Locate every uninfected red blood cell.
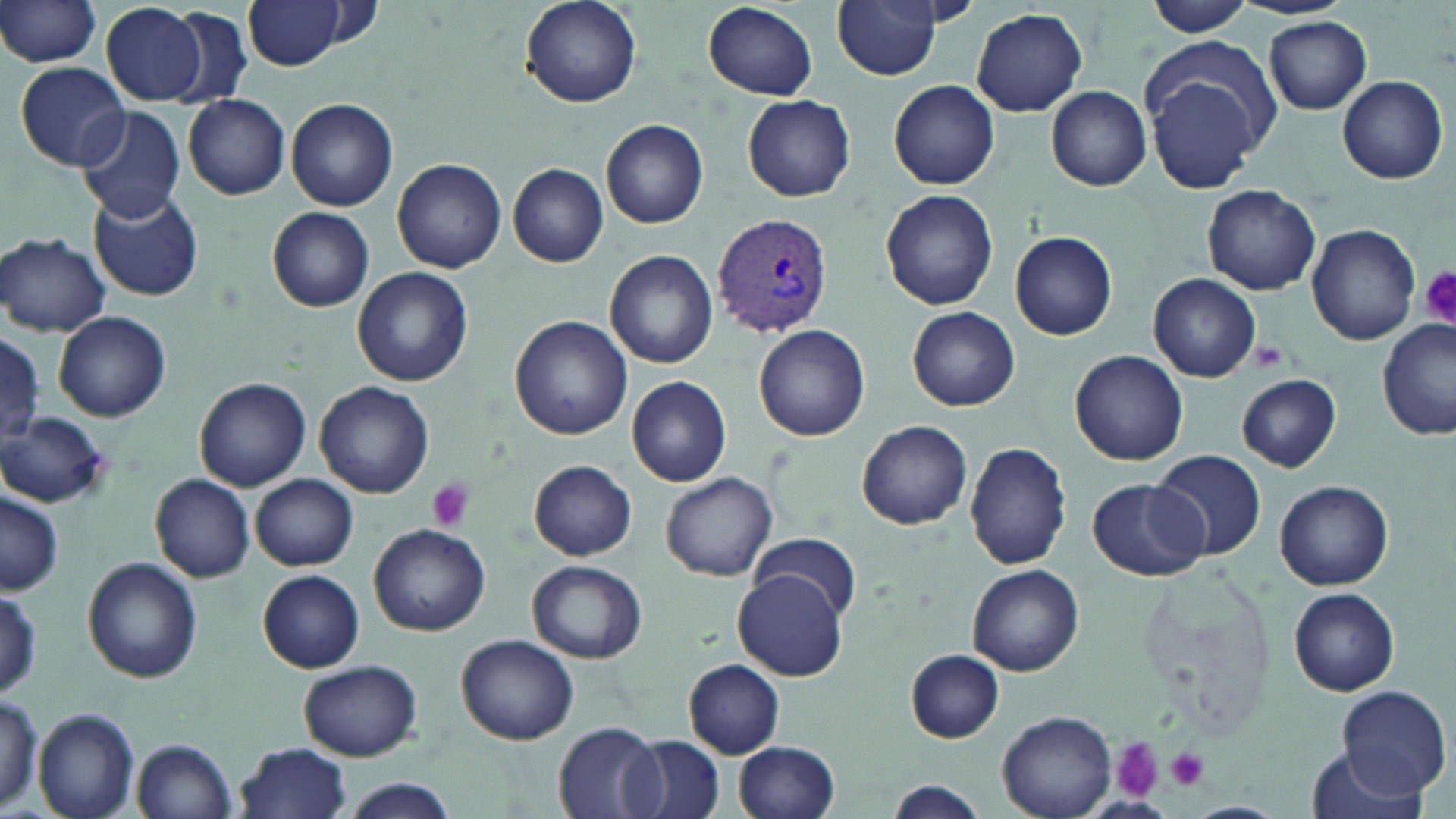
Approximate bounding boxes as [x1, y1, x2, y2] in pixels.
Uninfected red blood cells: [0, 0, 104, 68], [518, 0, 641, 108], [829, 0, 946, 82], [247, 1, 347, 69], [1143, 1, 1258, 36], [703, 2, 819, 101], [102, 4, 209, 107], [972, 8, 1089, 117], [165, 9, 253, 108], [1263, 17, 1373, 114], [1137, 39, 1280, 193], [15, 62, 130, 171], [1336, 75, 1448, 183], [889, 79, 1001, 189], [1046, 85, 1151, 190], [183, 94, 291, 200], [742, 95, 855, 202], [286, 99, 398, 211], [75, 106, 185, 223], [601, 118, 710, 229], [393, 157, 507, 274], [508, 163, 608, 267], [1202, 184, 1321, 295], [880, 188, 999, 311], [89, 191, 204, 302], [267, 207, 375, 311], [1308, 224, 1420, 345], [1009, 231, 1117, 341], [1, 233, 111, 336], [604, 251, 718, 368], [353, 268, 472, 386], [1148, 273, 1261, 382], [908, 307, 1020, 412], [54, 311, 171, 422], [510, 315, 633, 440], [1376, 319, 1454, 440], [753, 324, 870, 439], [0, 335, 45, 446], [1071, 352, 1189, 466], [1236, 373, 1342, 472], [193, 376, 311, 492], [626, 376, 732, 487], [315, 381, 434, 497], [0, 412, 110, 508], [856, 420, 972, 531], [965, 441, 1073, 572], [1152, 449, 1266, 561], [529, 459, 637, 561], [661, 471, 778, 581], [150, 473, 255, 582], [250, 475, 358, 570], [1086, 476, 1209, 582], [1275, 479, 1394, 590], [1, 491, 63, 595], [368, 523, 489, 635], [753, 532, 863, 621], [82, 557, 203, 682], [527, 561, 648, 664], [968, 564, 1082, 675], [735, 569, 848, 681], [258, 571, 365, 672], [1, 585, 44, 698], [1289, 587, 1400, 696], [457, 634, 578, 745], [905, 650, 1006, 742], [298, 659, 421, 760], [684, 659, 785, 757], [1335, 686, 1450, 797], [0, 691, 44, 814], [33, 708, 140, 819], [995, 711, 1118, 819], [554, 723, 662, 817], [621, 735, 724, 819], [131, 738, 238, 819], [733, 740, 841, 819], [235, 741, 352, 819], [1307, 746, 1434, 819], [340, 778, 459, 819], [884, 781, 986, 818], [1089, 794, 1180, 816], [1182, 801, 1285, 819].

Platelet locations: [1419, 267, 1456, 326], [1246, 340, 1291, 371], [425, 478, 476, 531], [1110, 737, 1162, 801], [1166, 745, 1209, 790]. Plasmodium vivax-infected red blood cell locations: [711, 214, 833, 337]. Slide-level diagnosis: Plasmodium vivax. Single field of view. Optical microscopy. Image is 1456×819 pixels. Thin blood smear. May-Grünwald-Giemsa stain. 1000x magnification.